Assess for Plasmodium parasites.
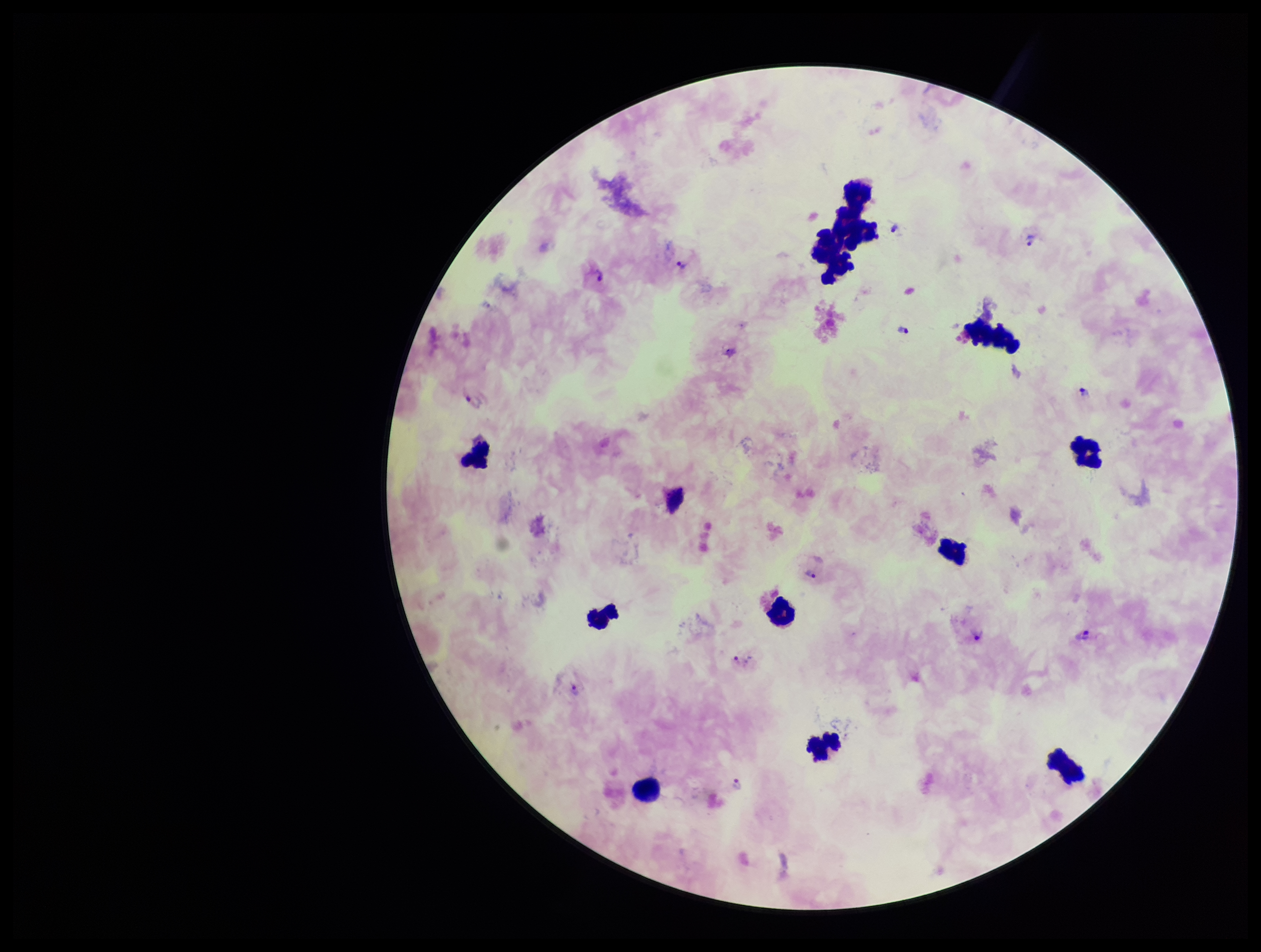
Detected.

stain = Giemsa
patient malaria status = infected
preparation = thick smear
capture = smartphone photograph through the microscope eyepiece
parasite count = 15
image size = 1261×952 pixels
field of view = single
species reported for this patient = Plasmodium vivax
leukocyte count = 12